Point out each Plasmodium parasite.
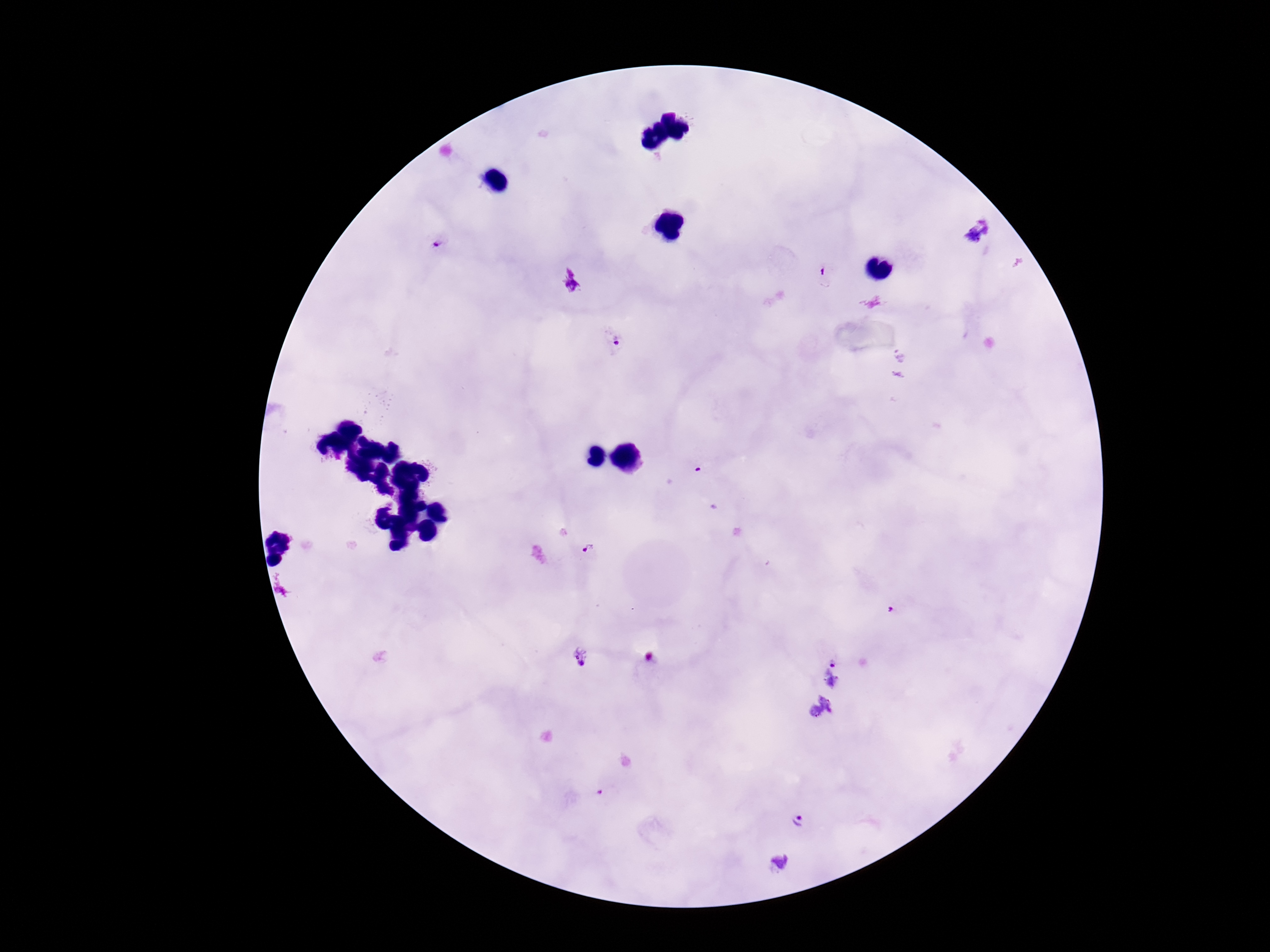
Approximate object centers, in pixels from the top-left corner.
Plasmodium parasites: (x=438, y=241), (x=825, y=275), (x=613, y=339), (x=589, y=550), (x=580, y=657), (x=833, y=660), (x=798, y=823).

Summary:
  - Preparation: thick peripheral-blood smear
  - Patient malaria status: positive
  - Field of view: one from this slide
  - Capture: smartphone camera through the microscope eyepiece
  - Magnification: 100x
  - Stain: Giemsa
  - Image size: 1270×952 pixels